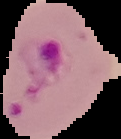
From a thin blood film. Segmented cell region on a black background. Result: Plasmodium parasites detected. Image is 121×139 pixels.